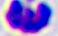
400x magnification. Micrograph. A leukocyte is shown.